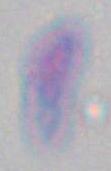

Summary:
  - Magnification: 1000x
  - Modality: photomicrograph
  - Identification: Toxoplasma gondii